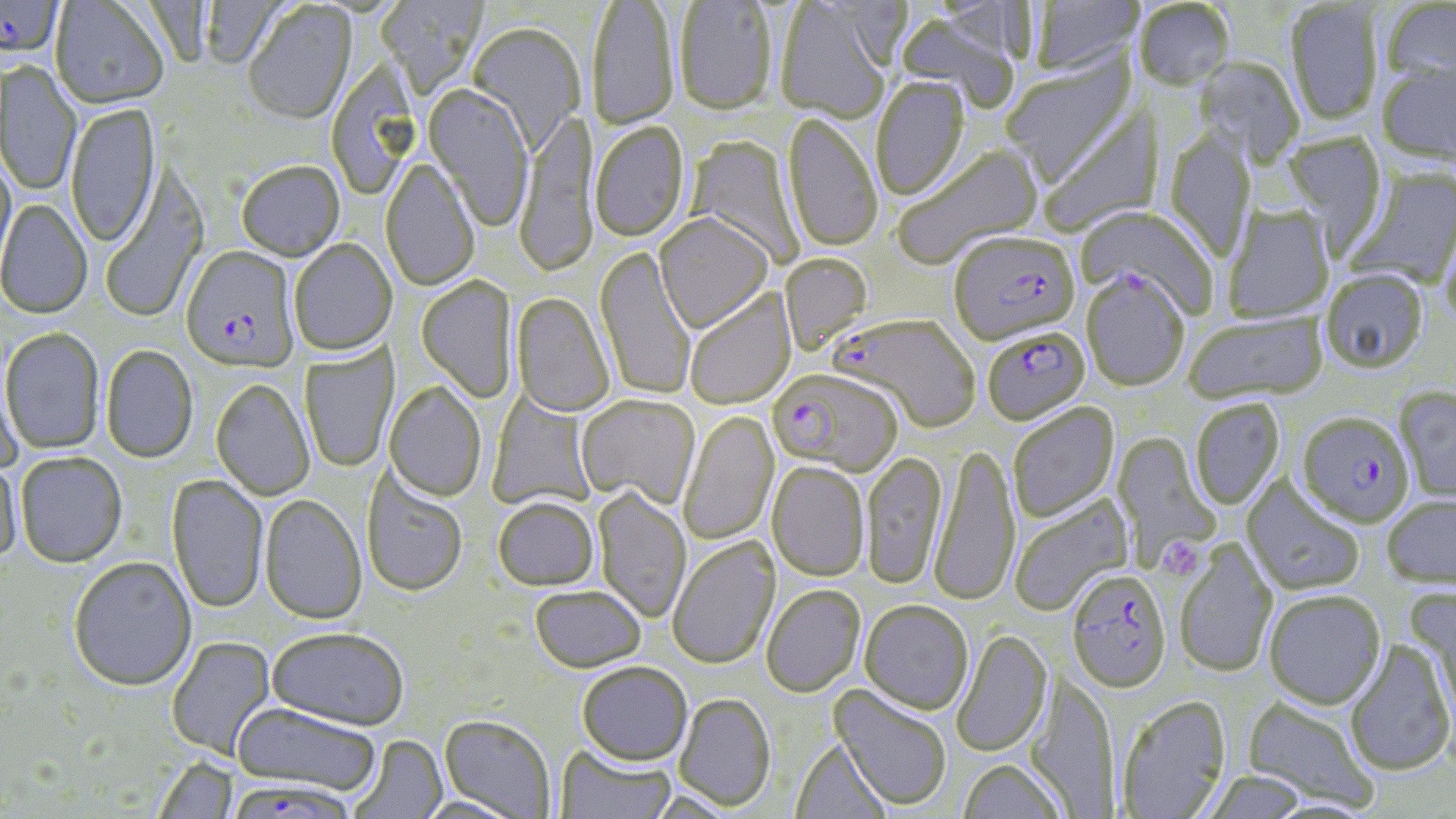

slide_level_diagnosis: Plasmodium falciparum
field_of_view: single
platelet_locations: 'approximate bounding boxes as [x1, y1, x2, y2] in pixels: [1157, 536, 1207, 582]'
preparation: thin blood smear
magnification: 1000x
stain: May-Grünwald-Giemsa
plasmodium_falciparum_infected_red_blood_cell_locations: 'approximate bounding boxes as [x1, y1, x2, y2] in pixels: [0, 0, 64, 63], [949, 233, 1080, 346], [180, 235, 298, 376], [1081, 272, 1189, 391], [832, 315, 981, 435], [982, 326, 1091, 426], [768, 368, 902, 474], [1296, 412, 1415, 528], [1066, 567, 1173, 694], [229, 778, 357, 819]'
uninfected_red_blood_cell_locations: 'approximate bounding boxes as [x1, y1, x2, y2] in pixels: [375, 0, 487, 97], [1031, 0, 1142, 76], [50, 1, 168, 111], [196, 1, 293, 71], [590, 1, 680, 132], [675, 1, 778, 118], [1380, 1, 1456, 86], [1135, 2, 1235, 93], [1285, 2, 1384, 128], [243, 3, 357, 126], [775, 3, 892, 123], [895, 11, 1022, 113], [467, 23, 585, 155], [1002, 53, 1139, 188], [1194, 58, 1304, 168], [2, 61, 82, 197], [1376, 64, 1456, 165], [871, 78, 971, 203], [424, 86, 533, 232], [1039, 100, 1165, 238], [66, 104, 162, 249], [515, 112, 598, 281], [783, 113, 882, 254], [590, 123, 689, 244], [1165, 129, 1257, 263], [1281, 132, 1387, 255], [684, 134, 804, 269], [893, 146, 1044, 269], [0, 153, 16, 276], [380, 159, 480, 292], [237, 162, 345, 262], [101, 166, 209, 324], [1344, 166, 1456, 291], [0, 199, 93, 319], [1077, 205, 1218, 319], [1223, 207, 1334, 323], [655, 215, 773, 335], [1439, 216, 1456, 335], [289, 240, 396, 356], [595, 246, 696, 402], [779, 253, 874, 354], [1320, 270, 1429, 375], [417, 277, 518, 403], [684, 289, 797, 410], [512, 293, 615, 418], [1184, 312, 1327, 404], [1, 327, 105, 455], [299, 343, 400, 473], [101, 345, 199, 463], [0, 359, 25, 475], [211, 379, 315, 501], [384, 382, 486, 502], [1394, 386, 1456, 503], [486, 391, 598, 512], [575, 395, 700, 509], [1190, 399, 1285, 510], [1007, 402, 1120, 523], [678, 409, 779, 546], [1112, 433, 1222, 571], [929, 445, 1021, 608], [15, 452, 127, 568], [861, 452, 947, 590], [0, 453, 23, 566], [767, 462, 870, 581], [361, 467, 469, 597], [167, 474, 268, 614], [1242, 478, 1366, 597], [592, 488, 692, 623], [1008, 494, 1134, 618], [259, 495, 367, 625], [1381, 495, 1456, 589], [493, 496, 599, 590], [667, 535, 780, 670], [1173, 539, 1278, 678], [68, 557, 197, 691], [529, 584, 646, 672], [760, 585, 865, 698], [1405, 585, 1456, 728], [1264, 590, 1386, 710], [860, 600, 973, 715], [267, 627, 409, 730], [951, 629, 1052, 758], [166, 636, 275, 761], [1344, 640, 1455, 776], [576, 662, 693, 765], [1026, 673, 1118, 817], [829, 685, 952, 812], [673, 692, 776, 811], [1116, 694, 1231, 818], [1243, 697, 1379, 811], [231, 702, 381, 798], [440, 714, 556, 818], [348, 735, 447, 819], [790, 737, 891, 819], [554, 742, 676, 819], [151, 756, 238, 818], [957, 758, 1069, 819], [1202, 771, 1308, 819], [415, 795, 526, 819]'
modality: light microscopy
image_size: 1456×819 pixels